Describe the morphology of the red blood cells.
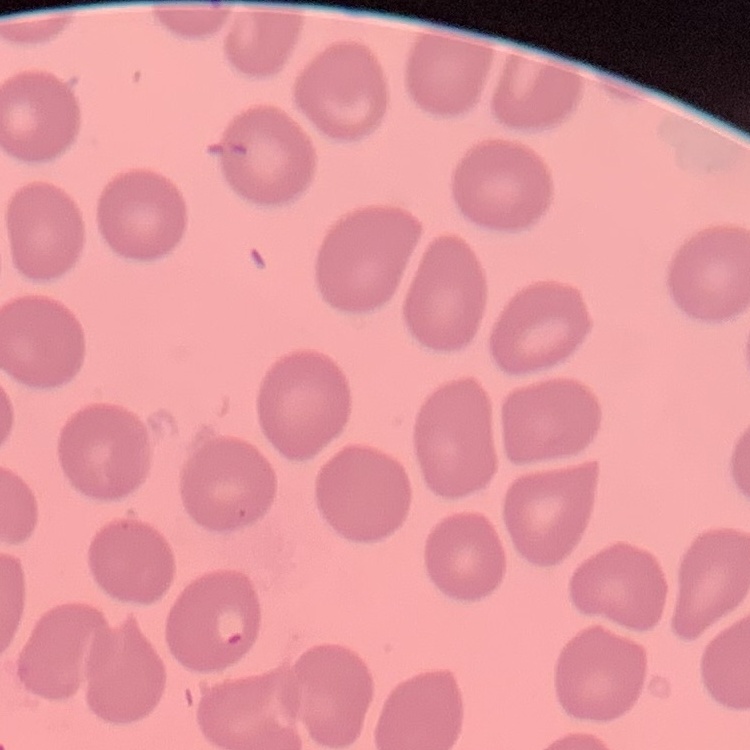

No rouleaux formation.

Square crop of a larger photomicrograph. Thin blood film. Stained with either Field's or Giemsa.